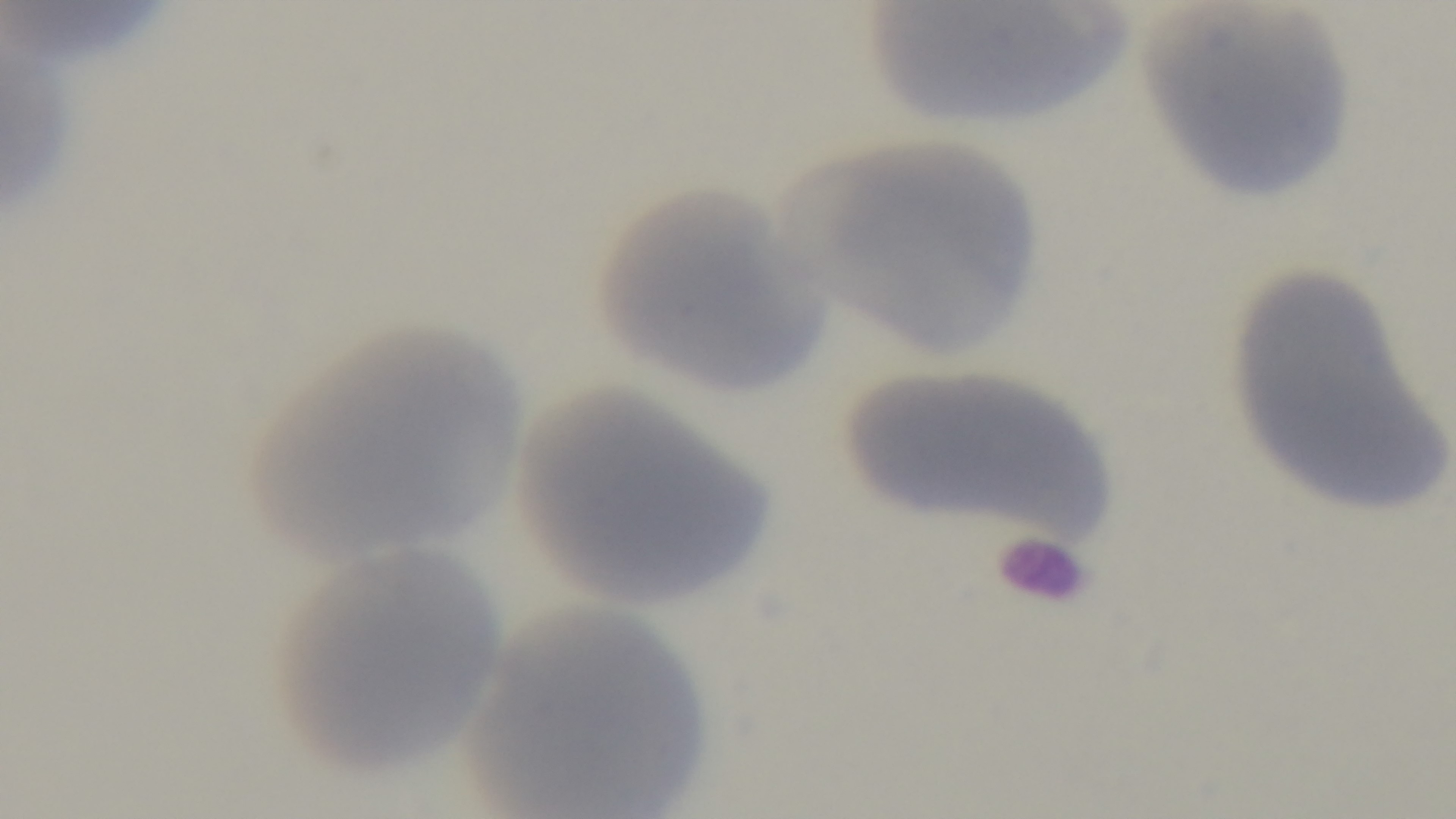

Summary:
  - Stain: Giemsa
  - Capture: mounted 4K digital camera
  - Modality: light microscopy
  - Malaria status: uninfected
  - Preparation: thin smear
  - Objective: 100x oil immersion
  - Field of view: single